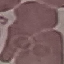

Malaria status: uninfected. Photographed with a smartphone camera at the microscope eyepiece. Giemsa stain. Cell patch, automatically extracted from a larger field of view and resized to 64 × 64 pixels. Thin blood film.